Give the preparation type.
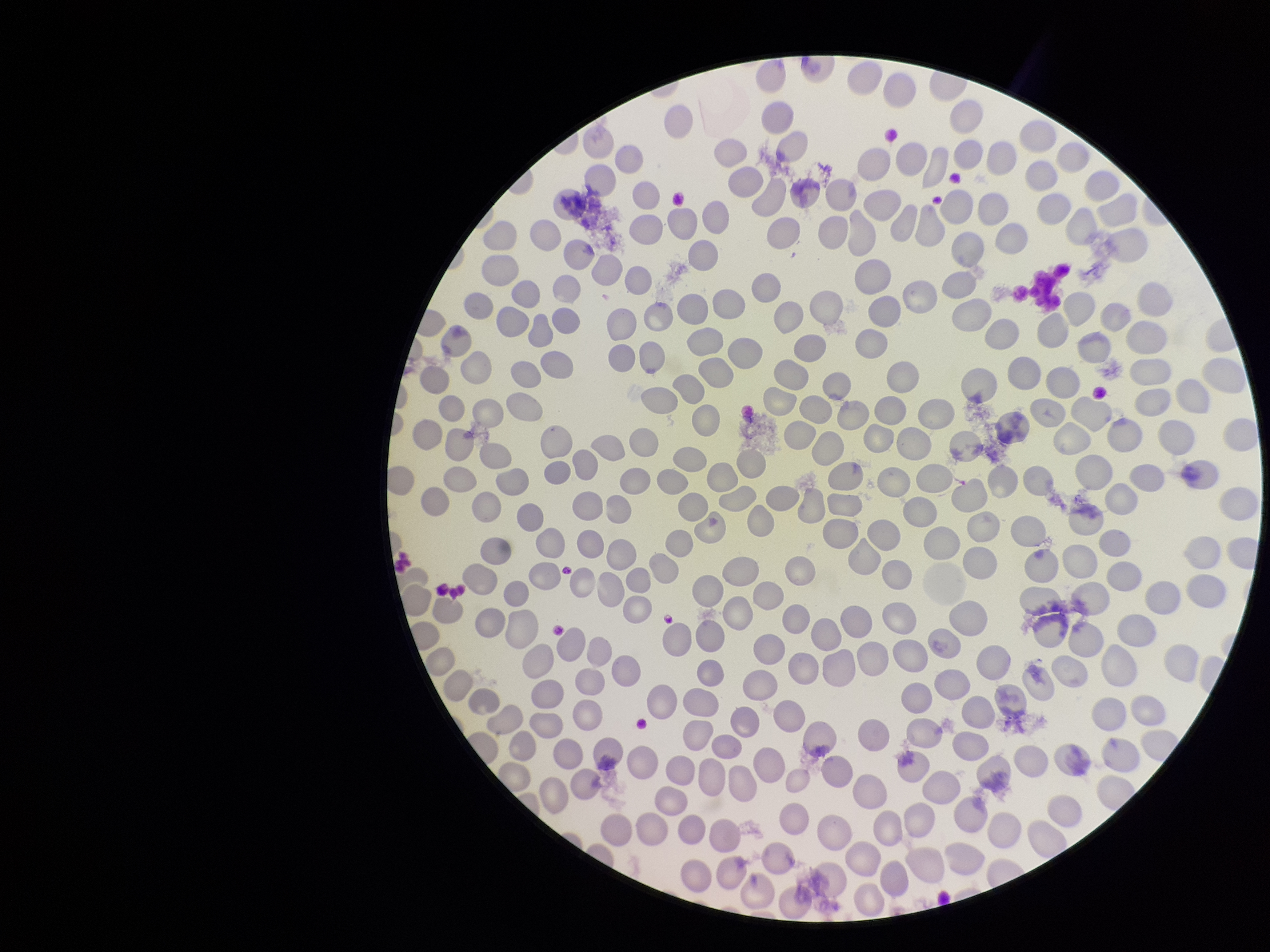

A thin smear.

field of view = single
parasitized red blood cells = none detected
red blood cell count = 304
species reported for this patient = Plasmodium falciparum
patient malaria status = positive
image size = 1270×952 pixels
capture = smartphone photograph through the microscope eyepiece
parasitized red blood cell count = 0
stain = Giemsa